Locate every Plasmodium ovale-infected red blood cell.
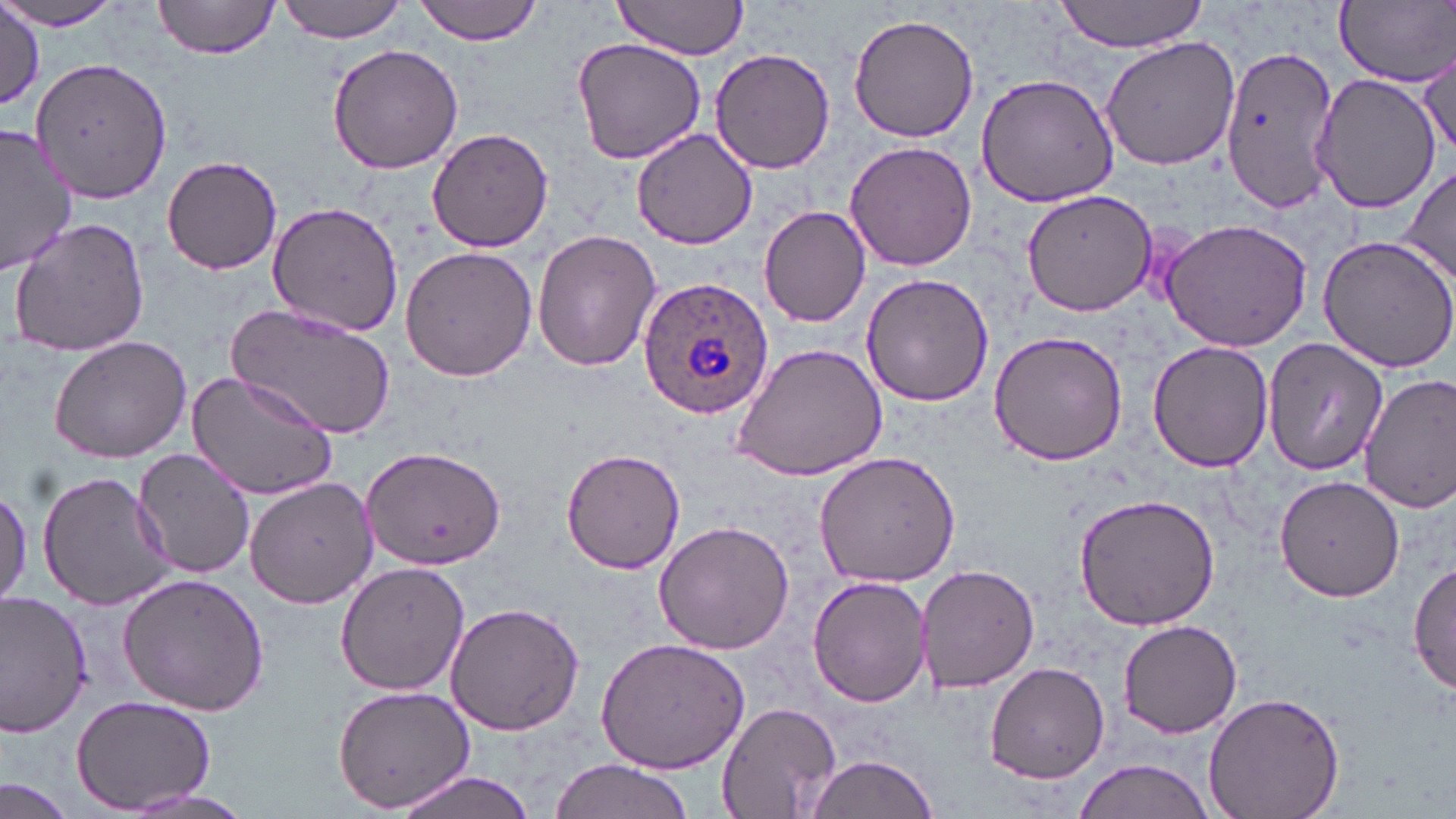

Approximate bounding boxes as [x1, y1, x2, y2] in pixels.
Plasmodium ovale-infected red blood cells: [636, 277, 775, 420].

slide-level diagnosis = Plasmodium ovale
field of view = single
image size = 1456×819 pixels
modality = optical microscopy
preparation = thin blood film
uninfected red blood cell locations = approximate bounding boxes as [x1, y1, x2, y2] in pixels: [151, 0, 283, 59], [278, 0, 409, 42], [412, 0, 546, 44], [1052, 0, 1211, 52], [610, 1, 750, 61], [1336, 1, 1455, 88], [0, 2, 127, 31], [1, 8, 43, 110], [848, 13, 980, 143], [1100, 36, 1243, 172], [572, 37, 706, 165], [325, 42, 467, 175], [1219, 44, 1342, 211], [709, 46, 837, 175], [1415, 46, 1453, 159], [30, 54, 171, 203], [1313, 72, 1441, 213], [975, 74, 1120, 209], [629, 126, 759, 248], [1, 127, 76, 274], [427, 129, 553, 252], [844, 140, 977, 271], [160, 155, 285, 274], [1403, 164, 1455, 290], [1019, 188, 1157, 317], [267, 201, 407, 334], [759, 205, 872, 327], [8, 216, 151, 357], [1160, 218, 1314, 353], [533, 231, 662, 371], [1317, 234, 1456, 373], [400, 245, 536, 381], [861, 273, 993, 407], [228, 302, 397, 440], [987, 330, 1130, 466], [48, 333, 190, 463], [1261, 338, 1388, 475], [1146, 340, 1274, 469], [729, 342, 888, 482], [185, 366, 341, 502], [1358, 374, 1456, 511], [359, 445, 506, 572], [135, 447, 257, 578], [560, 448, 688, 573], [812, 451, 961, 587], [37, 470, 175, 611], [1274, 475, 1404, 603], [245, 476, 379, 609], [0, 483, 30, 611], [1072, 492, 1220, 632], [651, 519, 796, 654], [1411, 558, 1455, 697], [916, 562, 1039, 693], [336, 563, 472, 695], [117, 572, 269, 715], [809, 574, 931, 707], [0, 594, 92, 737], [444, 601, 586, 735], [1120, 618, 1242, 738], [594, 636, 750, 773], [985, 663, 1112, 784], [332, 682, 478, 815], [1203, 691, 1346, 819], [70, 696, 217, 814], [718, 702, 842, 817], [803, 752, 941, 819], [547, 757, 699, 819], [1069, 758, 1219, 819], [390, 768, 544, 819], [0, 776, 77, 819], [110, 787, 257, 819]
stain = May-Grünwald-Giemsa
magnification = 1000x